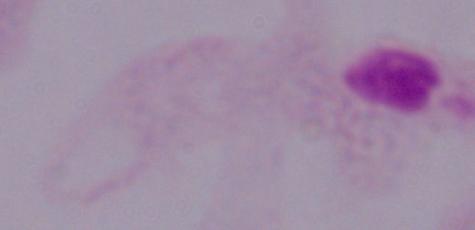 Captured at 1000x magnification. Photomicrograph. A trichomonad is shown.